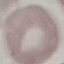
Summary:
  - Result: no malaria parasites detected
  - Image type: cell patch, automatically extracted from a larger field of view and resized to 64 × 64 pixels
  - Capture: smartphone through the microscope eyepiece
  - Preparation: thin blood smear
  - Stain: Giemsa